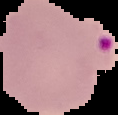
Image is 118×115 pixels. Malaria status: parasitized. From a thin blood smear. Segmented cell region on a black background.